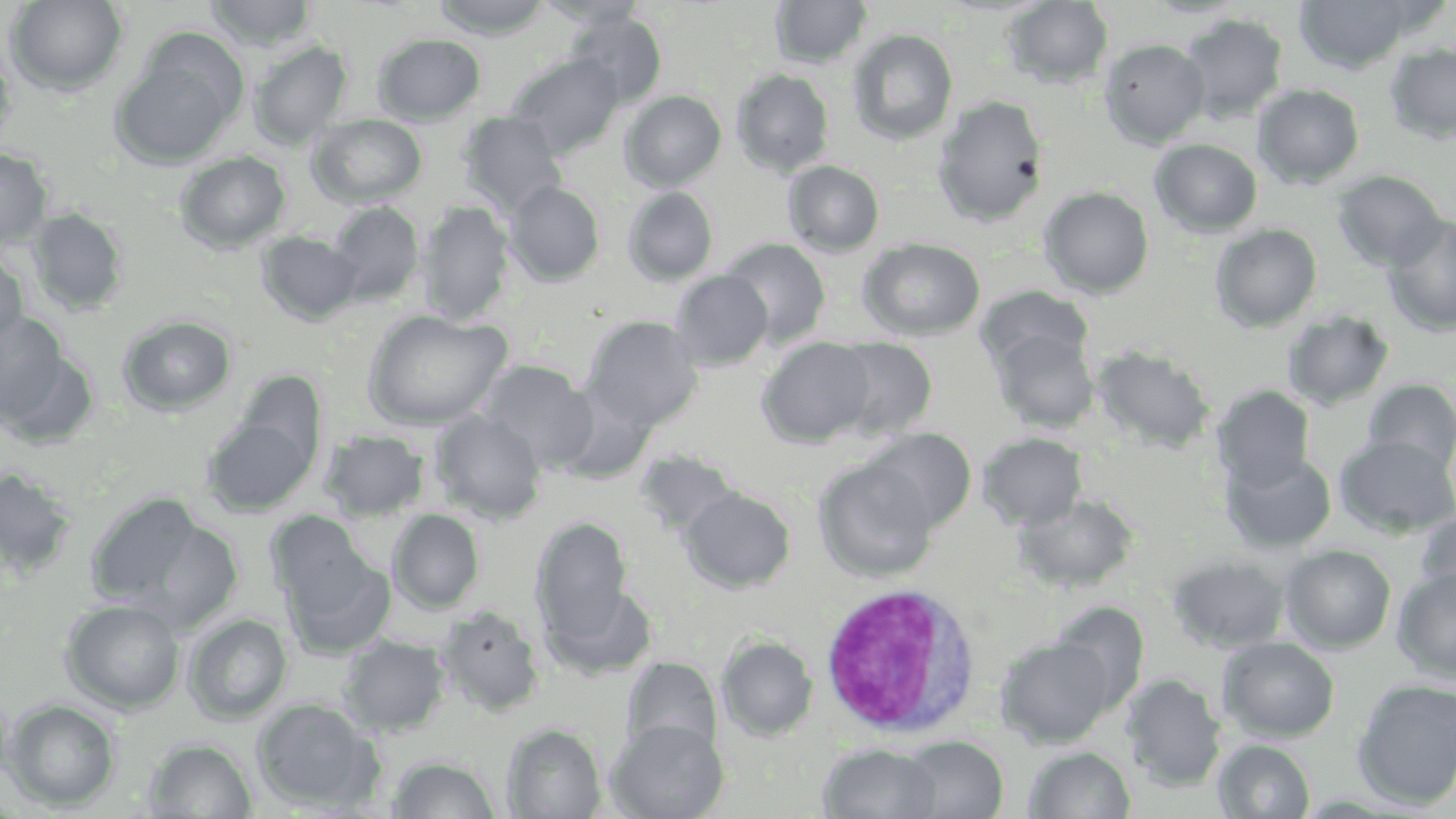 Approximate bounding boxes as (x1,y1)-(x2,y2) corner pairs in pixels. White blood cell locations: (818,584)-(985,740). Uninfected red blood cell locations: (4,0)-(128,95), (432,0)-(553,39), (534,0)-(649,28), (1143,0)-(1251,19), (1294,0)-(1417,74), (204,1)-(318,49), (769,1)-(871,69), (1002,1)-(1114,90), (566,10)-(667,108), (1179,13)-(1288,122), (847,28)-(959,145), (372,33)-(486,126), (1099,38)-(1211,148), (247,41)-(352,148), (1384,43)-(1456,144), (110,44)-(244,170), (0,46)-(18,154), (508,52)-(625,159), (731,68)-(835,177), (1252,84)-(1365,188), (620,90)-(726,191), (933,95)-(1048,227), (457,111)-(567,218), (307,113)-(428,208), (1149,139)-(1263,238), (0,149)-(53,250), (174,151)-(292,254), (784,160)-(885,257), (1332,170)-(1448,272), (504,181)-(605,287), (622,186)-(718,285), (1039,186)-(1155,298), (326,201)-(425,306), (416,201)-(515,326), (26,208)-(128,316), (1383,213)-(1456,337), (1210,224)-(1323,332), (256,231)-(362,325), (722,238)-(832,348), (859,238)-(986,341), (0,248)-(29,348), (670,270)-(773,370), (976,287)-(1094,379), (363,309)-(511,430), (0,311)-(77,433), (1282,311)-(1395,411), (118,314)-(237,416), (583,315)-(703,432), (990,327)-(1099,433), (757,337)-(877,447), (825,337)-(938,441), (1091,345)-(1215,454), (477,360)-(598,472), (1363,378)-(1456,472), (1214,385)-(1315,490), (201,409)-(320,517), (429,410)-(547,523), (864,428)-(976,533), (319,430)-(430,522), (978,432)-(1088,530), (1335,434)-(1456,538), (634,449)-(741,543), (1222,450)-(1337,554), (813,458)-(939,582), (0,466)-(78,580), (679,486)-(796,593), (86,492)-(224,619), (1015,492)-(1141,593), (388,508)-(485,613), (266,510)-(374,614), (1415,510)-(1456,610), (532,517)-(633,642), (1281,544)-(1397,652), (281,547)-(396,659), (1167,554)-(1290,653), (1393,566)-(1456,682), (546,581)-(658,680), (60,599)-(186,714), (1048,603)-(1150,715), (436,606)-(545,717), (183,613)-(293,725), (340,635)-(450,736), (717,636)-(818,741), (995,636)-(1119,748), (1217,636)-(1340,742), (623,657)-(721,759), (1122,673)-(1227,791), (1351,678)-(1456,810), (252,698)-(383,813), (3,699)-(121,812), (607,718)-(728,819), (503,724)-(605,818), (900,736)-(1007,819), (144,738)-(257,818), (1212,739)-(1316,818), (819,744)-(941,818), (1024,746)-(1136,818), (386,755)-(502,818). Slide-level diagnosis: negative for blood parasites. One field of a larger specimen. Light microscopy. May-Grünwald-Giemsa stain. Image is 1456×819 pixels. Captured at 1000x magnification. Thin blood smear.